Assess this cell for malaria.
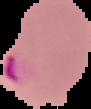
Parasitized.

Summary:
  - Image type: segmented cell region on a black background
  - Image size: 91×109 pixels
  - Preparation: thin blood smear